Assess the morphology of the erythrocytes.
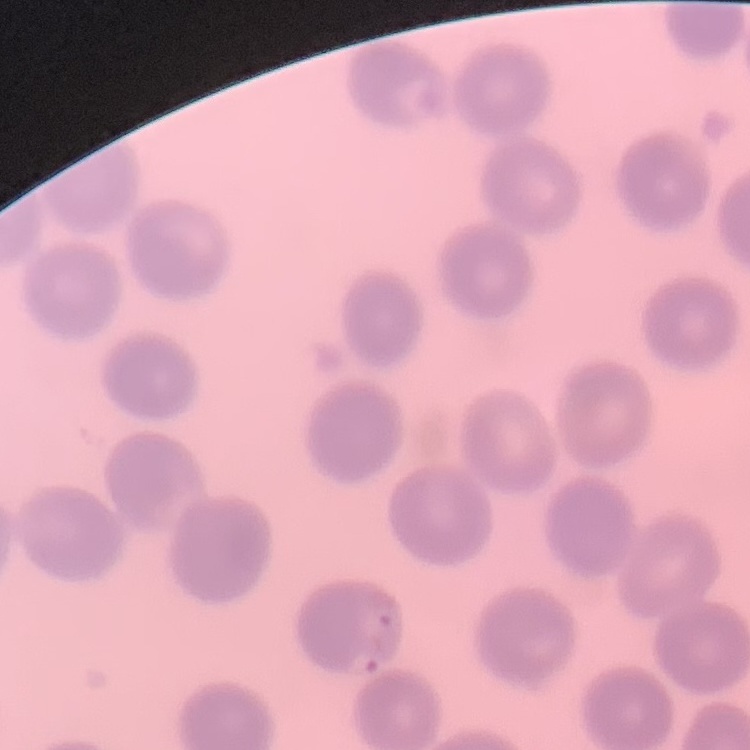
No rouleaux formation.

Summary:
  - Preparation: thin peripheral smear
  - Image type: one tile cut from a larger photomicrograph
  - Stain: Field's or Giemsa